Locate every blood parasite and identify its species.
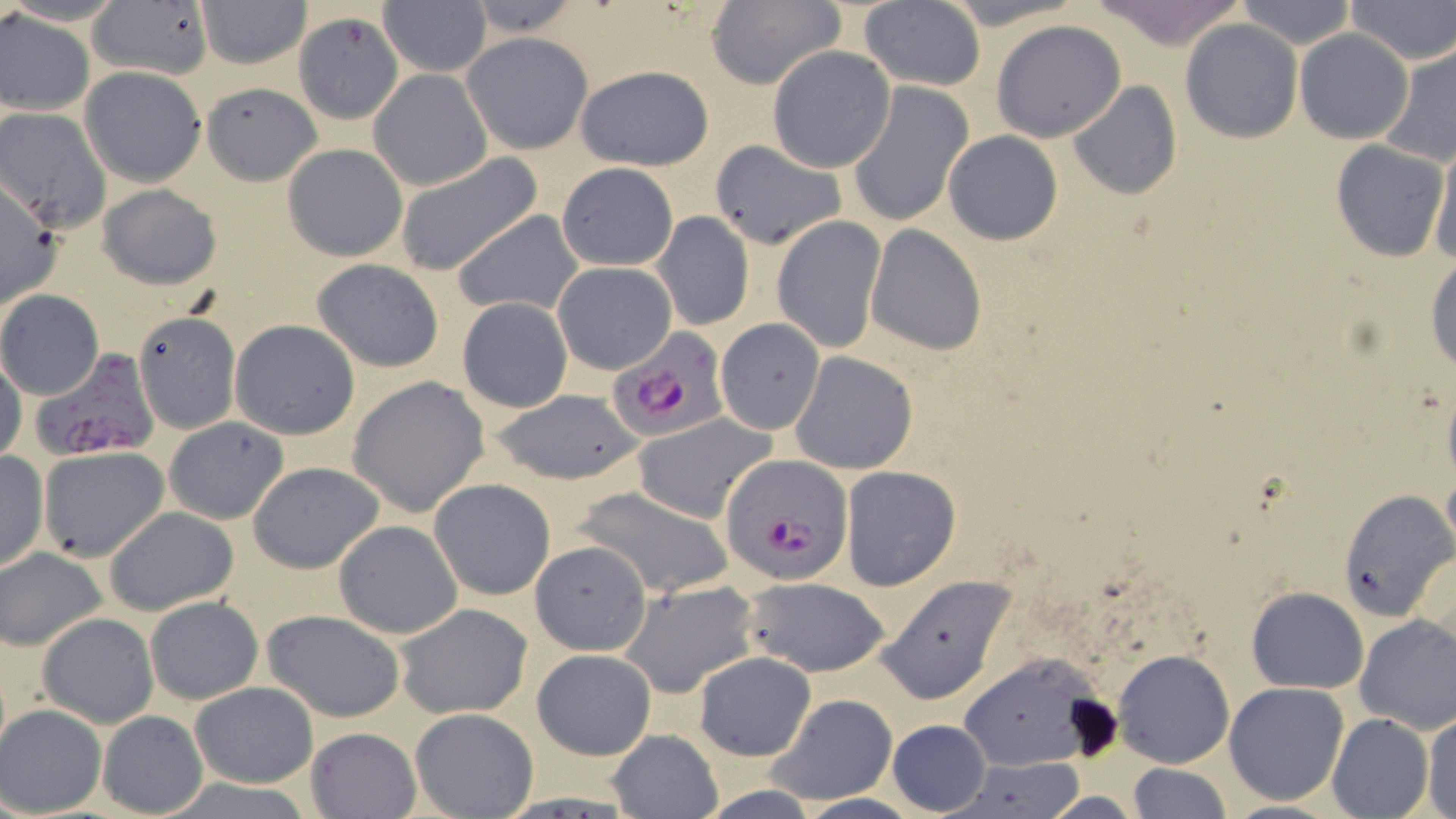
Approximate bounding boxes as [x1, y1, x2, y2] in pixels.
Plasmodium falciparum-infected red blood cells: [608, 332, 727, 442], [32, 351, 162, 463], [722, 457, 854, 585].
No Plasmodium ovale, Plasmodium malariae, Plasmodium vivax, Babesia divergens, or Trypanosoma brucei observed.

Uninfected red blood cell locations: [87, 0, 213, 81], [462, 0, 589, 40], [704, 0, 846, 91], [1091, 0, 1247, 48], [1235, 0, 1357, 49], [1343, 0, 1454, 65], [195, 1, 312, 68], [379, 2, 492, 78], [858, 2, 986, 90], [0, 9, 96, 117], [292, 11, 401, 123], [991, 19, 1126, 142], [1179, 19, 1302, 142], [1295, 29, 1413, 143], [463, 32, 593, 155], [1380, 43, 1456, 167], [767, 45, 897, 173], [574, 64, 715, 170], [79, 65, 207, 187], [369, 69, 492, 190], [1067, 80, 1181, 200], [200, 81, 323, 185], [846, 84, 973, 227], [0, 109, 112, 232], [943, 131, 1063, 245], [1428, 133, 1456, 266], [709, 138, 847, 248], [1329, 139, 1448, 261], [283, 143, 409, 261], [392, 152, 543, 277], [556, 163, 678, 271], [0, 179, 63, 311], [99, 183, 220, 289], [451, 209, 584, 317], [651, 210, 754, 332], [771, 215, 887, 353], [865, 224, 987, 355], [1426, 254, 1456, 375], [311, 258, 444, 372], [553, 262, 676, 375], [0, 290, 104, 399], [457, 297, 572, 413], [133, 309, 243, 432], [715, 318, 824, 434], [230, 319, 362, 440], [791, 350, 918, 474], [0, 352, 26, 467], [348, 375, 489, 517], [488, 389, 644, 487], [634, 414, 777, 523], [162, 417, 289, 524], [38, 447, 168, 563], [0, 450, 49, 572], [247, 461, 385, 575], [840, 466, 961, 592], [430, 478, 556, 601], [574, 484, 737, 600], [1337, 490, 1453, 619], [103, 506, 240, 615], [333, 519, 464, 638], [528, 540, 652, 656], [1, 547, 109, 651], [878, 574, 1014, 704], [739, 577, 892, 676], [620, 579, 759, 698], [1245, 585, 1369, 693], [145, 596, 263, 705], [394, 604, 534, 719], [263, 609, 404, 721], [37, 612, 160, 728], [1353, 613, 1456, 734], [531, 648, 656, 760], [1112, 648, 1234, 768], [962, 649, 1108, 769], [692, 651, 817, 761], [189, 681, 318, 788], [1224, 682, 1349, 805], [767, 693, 897, 804], [0, 704, 109, 817], [409, 707, 539, 818], [97, 710, 208, 817], [1422, 712, 1456, 819], [1326, 713, 1434, 819], [886, 719, 991, 815], [305, 727, 423, 817], [606, 728, 725, 819], [950, 759, 1088, 817], [1125, 763, 1232, 819]. Slide-level diagnosis: Plasmodium falciparum. Single field of view. May-Grünwald-Giemsa-stained preparation. Captured at 1000x magnification. Optical microscopy. Thin blood film. Image is 1456×819 pixels.